Name the parasite shown.
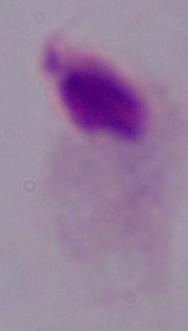

This is a trichomonad.

{
  "magnification": "1000x",
  "modality": "micrograph"
}